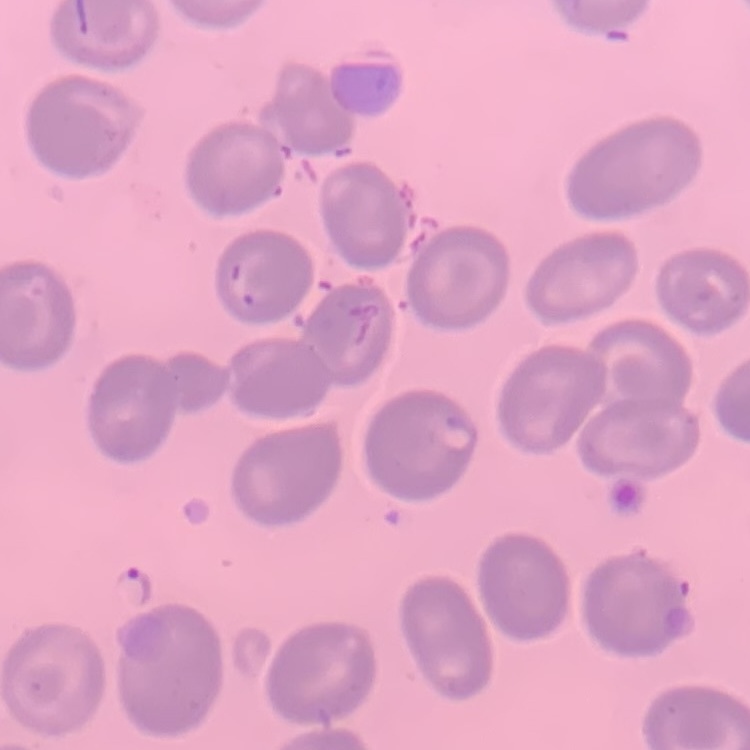
erythrocyte_morphology: no rouleaux formation
stain: Field's or Giemsa
preparation: thin blood film
image_type: square crop of a larger photomicrograph